Comment on the morphology of the red blood cells.
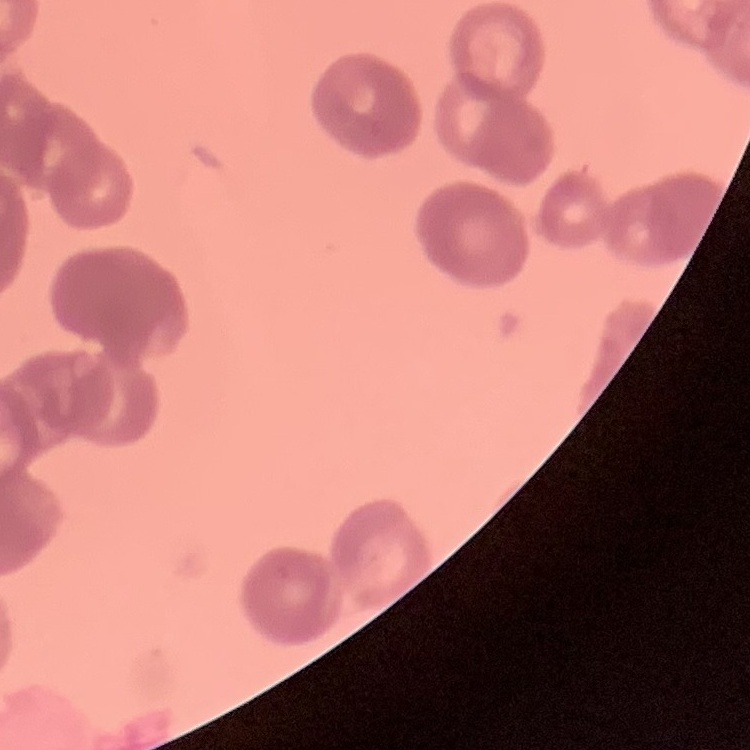
They show rouleaux formation.

Summary:
  - Stain: Field's or Giemsa
  - Image type: one tile cut from a larger photomicrograph
  - Preparation: thin peripheral smear